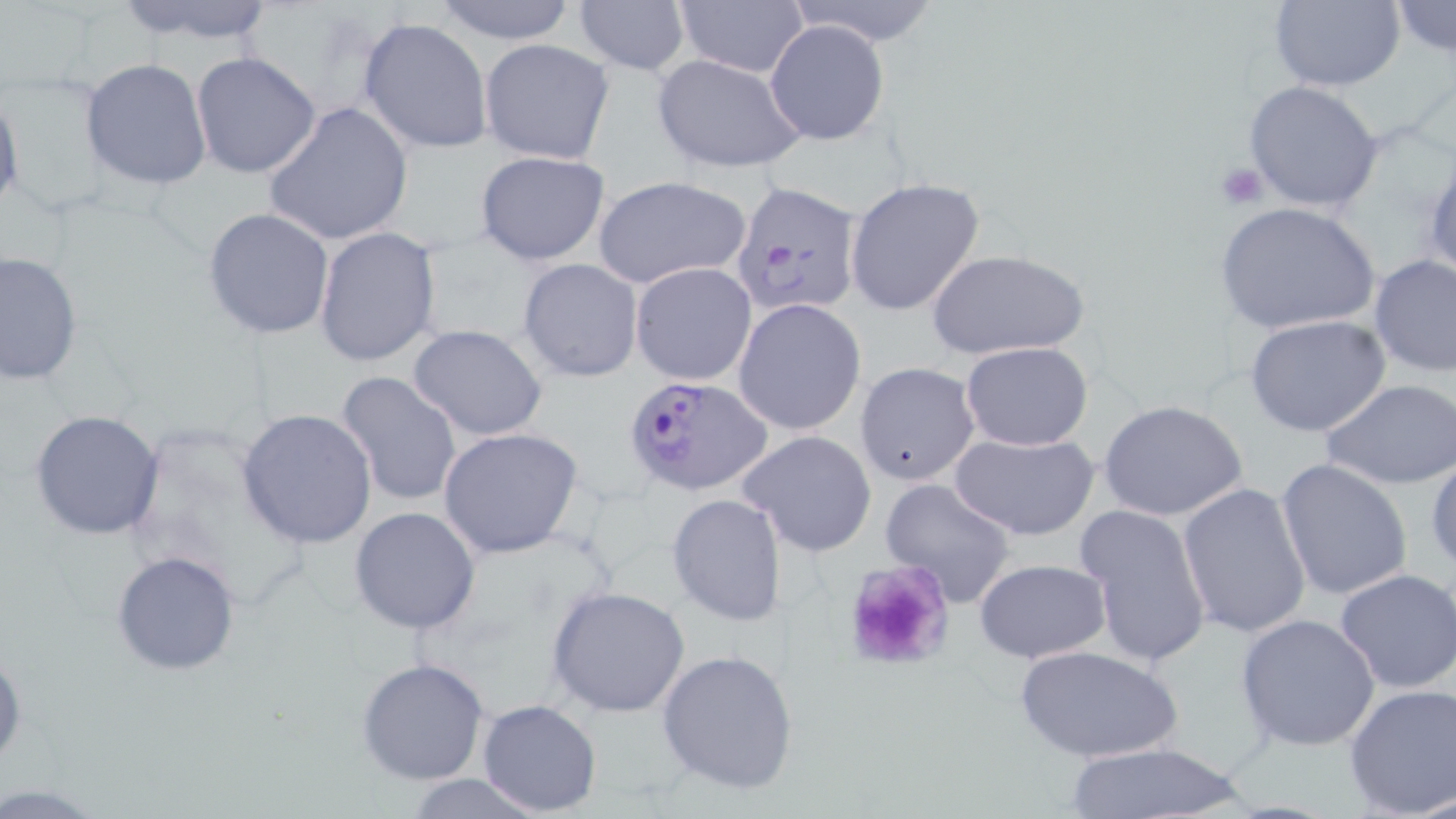

Approximate bounding boxes as (x1,y1)-(x2,y2) corner pairs in pixels. Uninfected red blood cell locations: (110,0)-(280,48), (429,0)-(580,45), (573,0)-(691,77), (786,0)-(942,47), (1267,0)-(1406,92), (675,1)-(808,77), (1388,2)-(1454,57), (358,16)-(493,155), (765,20)-(890,146), (479,38)-(614,165), (190,51)-(323,179), (652,53)-(807,173), (80,58)-(213,190), (1242,80)-(1386,214), (0,85)-(24,222), (264,101)-(413,247), (475,150)-(611,266), (1423,150)-(1456,286), (592,175)-(751,289), (845,176)-(986,317), (1214,201)-(1381,336), (201,207)-(335,340), (313,227)-(442,368), (926,248)-(1090,361), (0,251)-(82,388), (1368,253)-(1455,377), (517,258)-(643,382), (631,261)-(757,386), (733,298)-(867,436), (1244,314)-(1392,438), (407,324)-(551,441), (959,341)-(1094,451), (856,361)-(981,487), (334,370)-(461,509), (1323,379)-(1456,489), (1097,398)-(1249,523), (237,408)-(379,548), (29,409)-(166,541), (438,426)-(585,560), (737,429)-(878,558), (949,430)-(1101,541), (1427,451)-(1456,576), (1275,458)-(1413,600), (880,478)-(1018,607), (1178,482)-(1312,639), (666,493)-(785,628), (1074,504)-(1210,670), (350,506)-(481,633), (110,550)-(242,676), (971,559)-(1112,663), (1335,568)-(1456,693), (547,586)-(693,718), (1236,613)-(1381,752), (1014,643)-(1185,765), (0,647)-(26,773), (656,647)-(800,796), (356,657)-(490,785), (1342,682)-(1455,819), (477,699)-(603,816), (1056,742)-(1253,819), (398,774)-(557,818), (0,783)-(103,814). Plasmodium falciparum-infected red blood cell locations: (728,178)-(864,319), (622,373)-(772,496). Platelet locations: (1214,163)-(1267,211), (839,562)-(951,668). Slide-level diagnosis: Plasmodium falciparum. May-Grünwald-Giemsa stain. Single field of view. Image is 1456×819 pixels. Optical microscopy. Thin blood film. Captured at 1000x magnification.